Describe the morphology of the red blood cells.
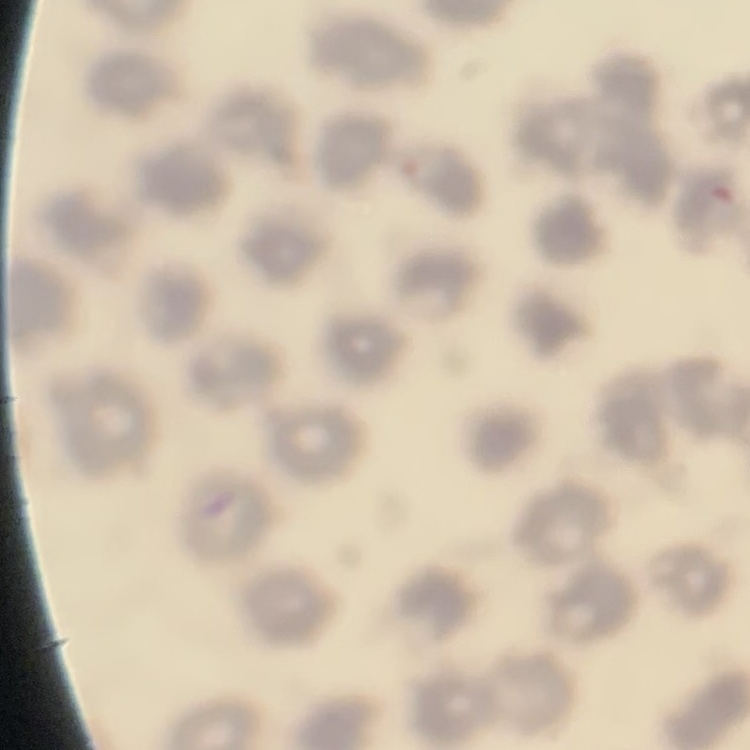
They show no rouleaux formation.

image type = one tile cut from a larger photomicrograph
preparation = thin blood film
stain = Field's or Giemsa